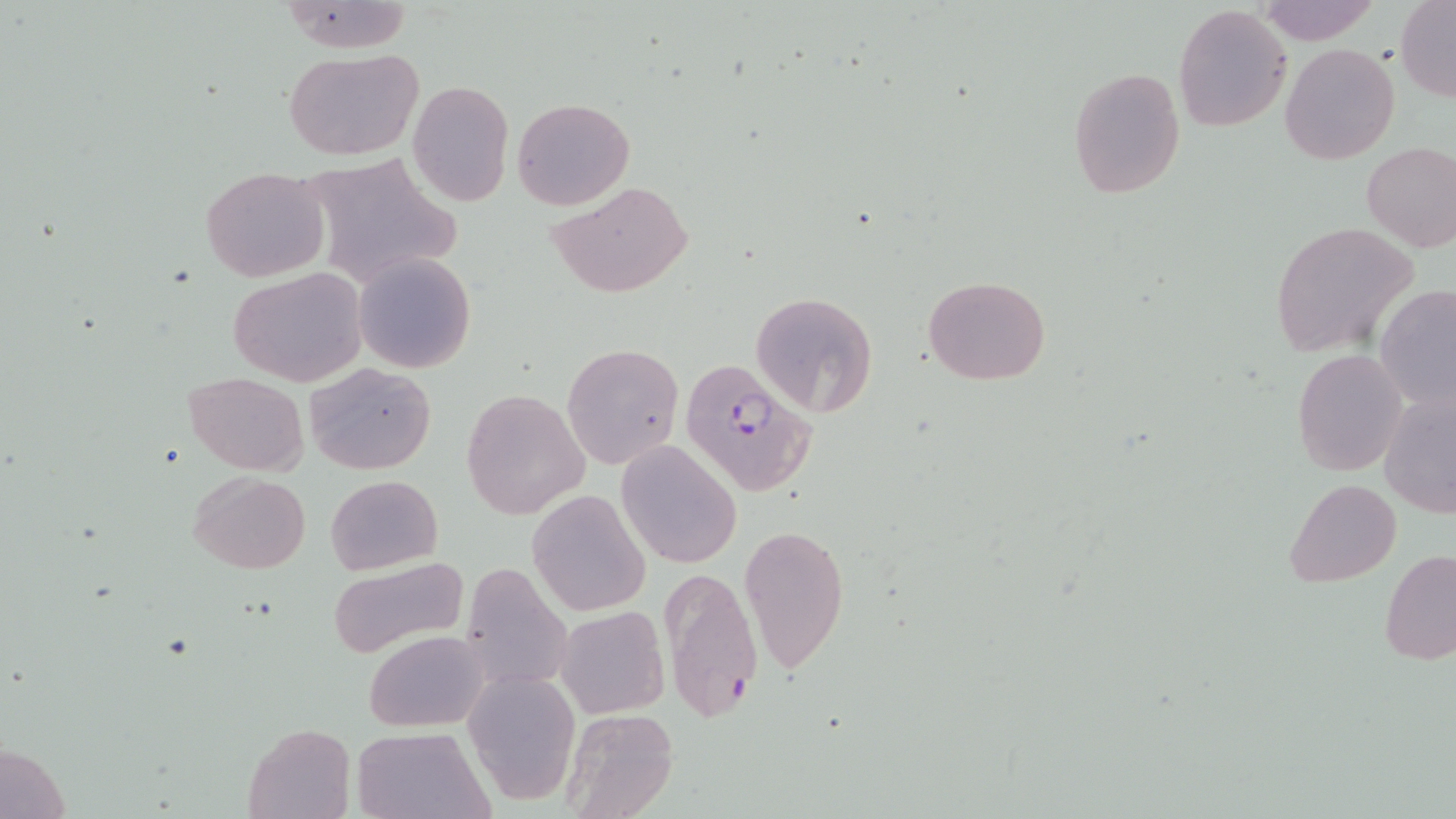

Summary:
  - Coordinate format: approximate bounding boxes as (x1, y1, x2, y2) in pixels
  - Plasmodium falciparum-infected red blood cell locations: (679, 358, 818, 498)
  - Uninfected red blood cell locations: (1253, 0, 1385, 46), (278, 1, 415, 52), (1397, 1, 1456, 101), (1173, 4, 1292, 133), (1282, 43, 1400, 164), (284, 48, 423, 161), (1066, 66, 1186, 199), (408, 79, 513, 205), (512, 97, 635, 209), (1361, 142, 1456, 253), (201, 167, 330, 281), (550, 179, 693, 299), (1269, 221, 1420, 361), (354, 251, 475, 374), (229, 267, 369, 387), (923, 277, 1050, 386), (1375, 285, 1456, 411), (751, 291, 879, 416), (561, 341, 684, 470), (1292, 348, 1410, 477), (305, 360, 436, 475), (183, 371, 309, 474), (1377, 387, 1455, 523), (462, 389, 589, 520), (616, 441, 741, 569), (187, 471, 313, 574), (326, 474, 442, 575), (1285, 479, 1401, 587), (528, 489, 651, 615), (738, 525, 850, 673), (1380, 548, 1456, 664), (327, 554, 471, 658), (458, 564, 575, 697), (659, 564, 761, 724), (556, 605, 670, 719), (361, 629, 488, 732), (467, 672, 578, 803), (561, 707, 678, 819), (243, 721, 357, 818), (351, 727, 492, 818)
  - Slide-level diagnosis: Plasmodium falciparum
  - Magnification: 1000x
  - Modality: optical microscopy
  - Stain: May-Grünwald-Giemsa
  - Preparation: thin blood film
  - Image size: 1456×819 pixels
  - Field of view: single